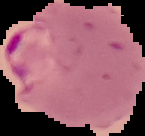

image size = 145×136 pixels
preparation = thin blood smear
image type = cell region segmented out of the field of view; surrounding area masked to black
malaria status = parasitized